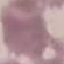
Summary:
  - Malaria status: uninfected
  - Stain: Giemsa
  - Capture: smartphone through the microscope eyepiece
  - Preparation: thin blood smear
  - Image type: automatically extracted cell patch, resized to 64 × 64 pixels